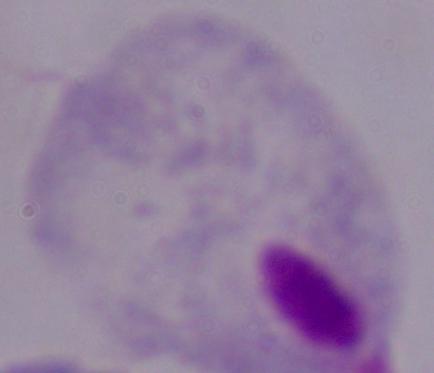 1000x magnification. A trichomonad is seen. Photomicrograph.